Identify the parasite.
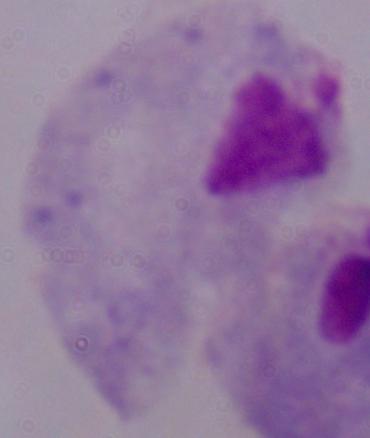

A trichomonad.

{
  "magnification": "1000x",
  "modality": "micrograph"
}